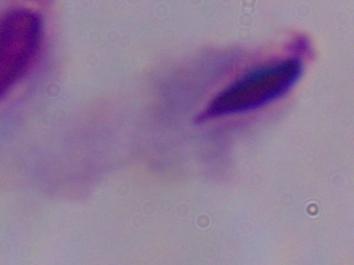 Micrograph. Captured at 1000x magnification. A trichomonad is seen.